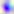
identification = Toxoplasma gondii
magnification = 400x
modality = micrograph